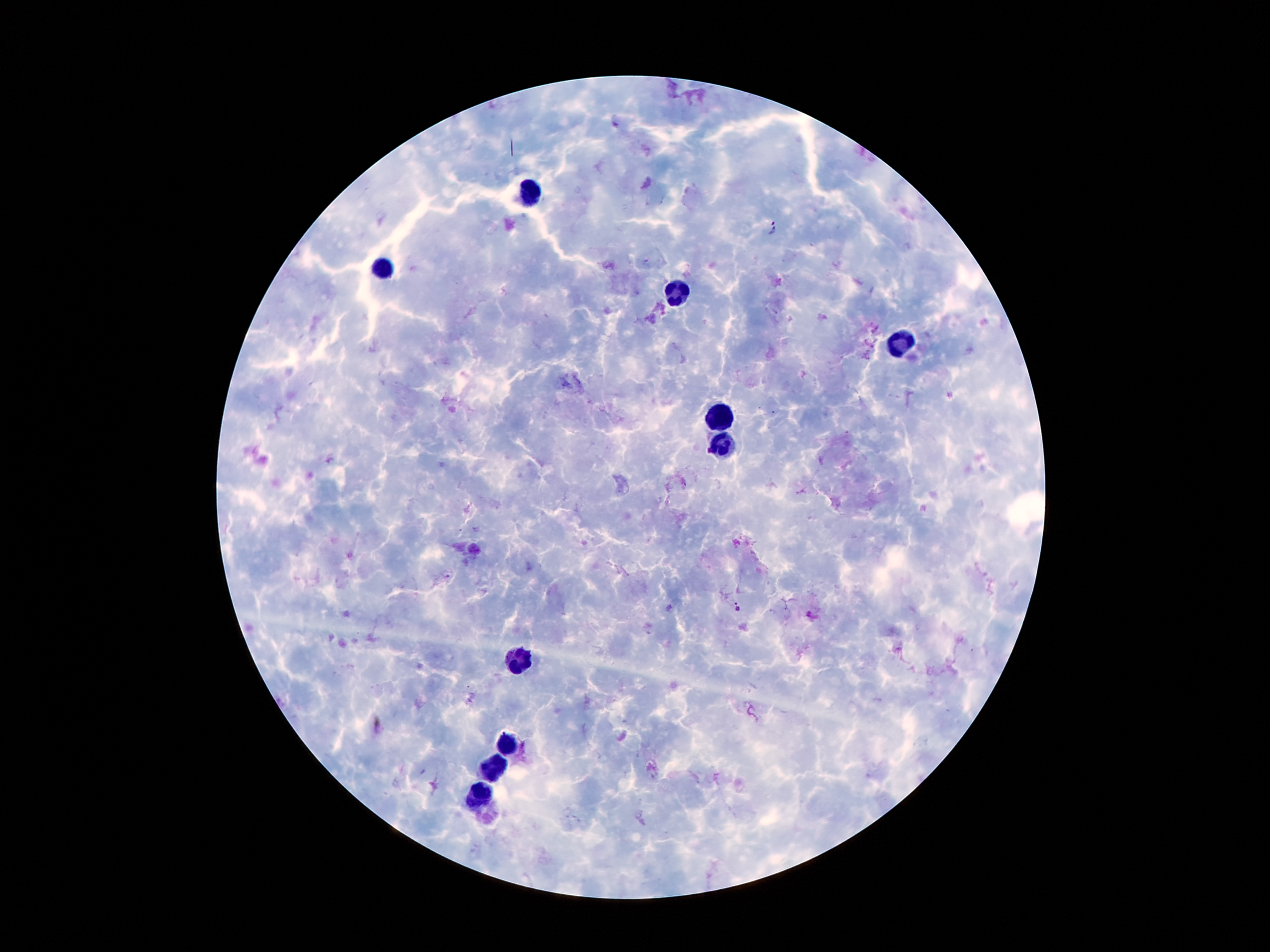

Approximate centers as {x, y} in pixels.
Summary:
  - Leukocyte locations: {529, 188}, {385, 267}, {675, 292}, {897, 342}, {723, 415}, {723, 444}, {515, 660}, {510, 742}, {498, 765}, {484, 795}
  - Plasmodium parasite locations: {772, 232}, {738, 606}
  - Stain: Giemsa
  - Patient malaria status: positive for Plasmodium falciparum
  - Preparation: thick blood smear
  - Image size: 1270×952 pixels
  - Capture: smartphone camera through the microscope eyepiece
  - Field of view: one from this slide
  - Magnification: 100x